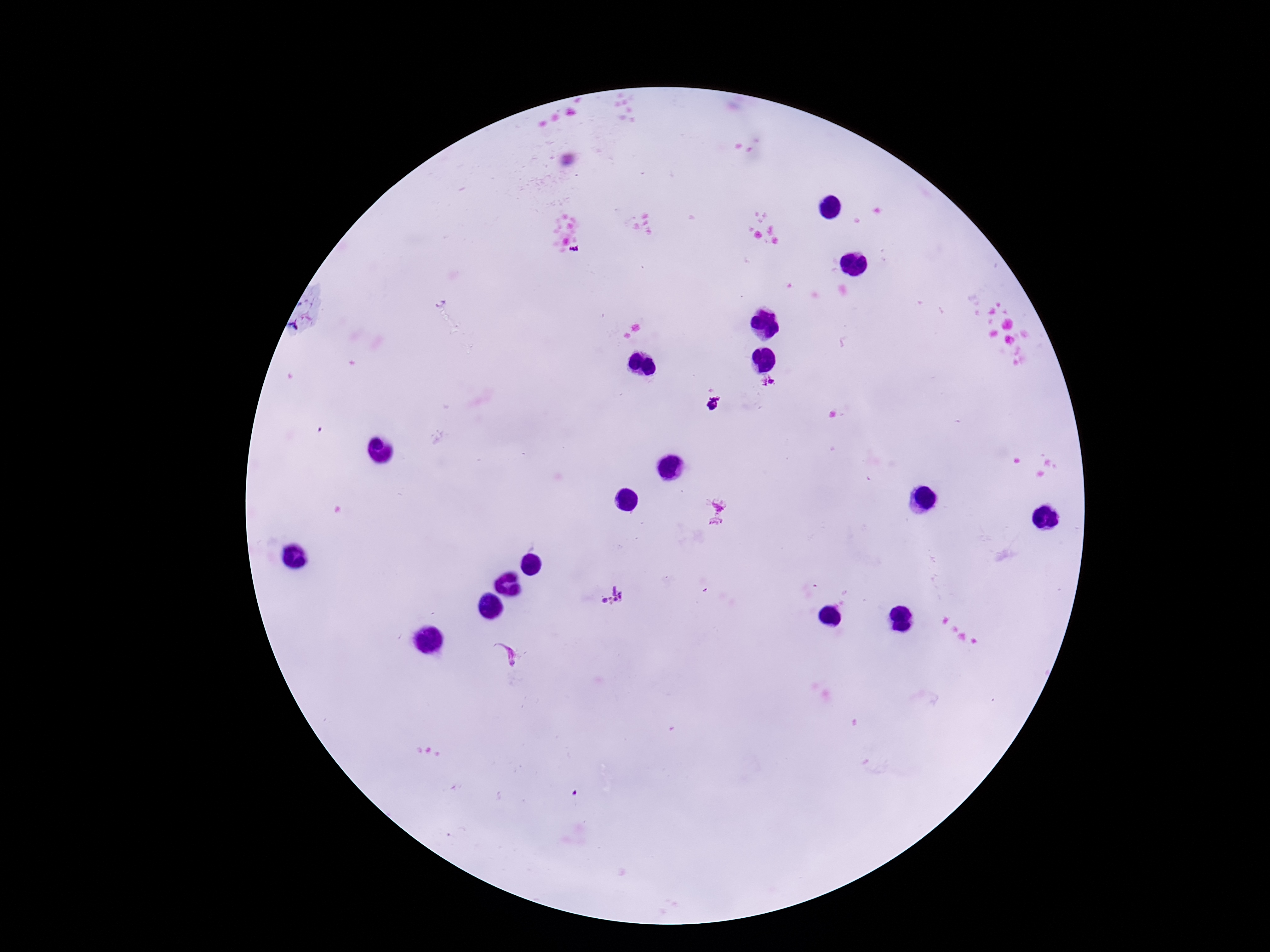 Approximate centers as {x, y} in pixels. Plasmodium parasite locations: {768, 382}, {713, 404}, {716, 512}, {611, 597}, {505, 654}. Image is 1270×952 pixels. Smartphone photograph taken through the microscope eyepiece. Patient malaria status: infected. Thick peripheral-blood smear. Giemsa stain. Single field of view. 100x magnification.